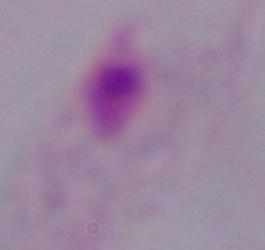

Summary:
  - Modality: micrograph
  - Identification: trichomonad
  - Magnification: 1000x